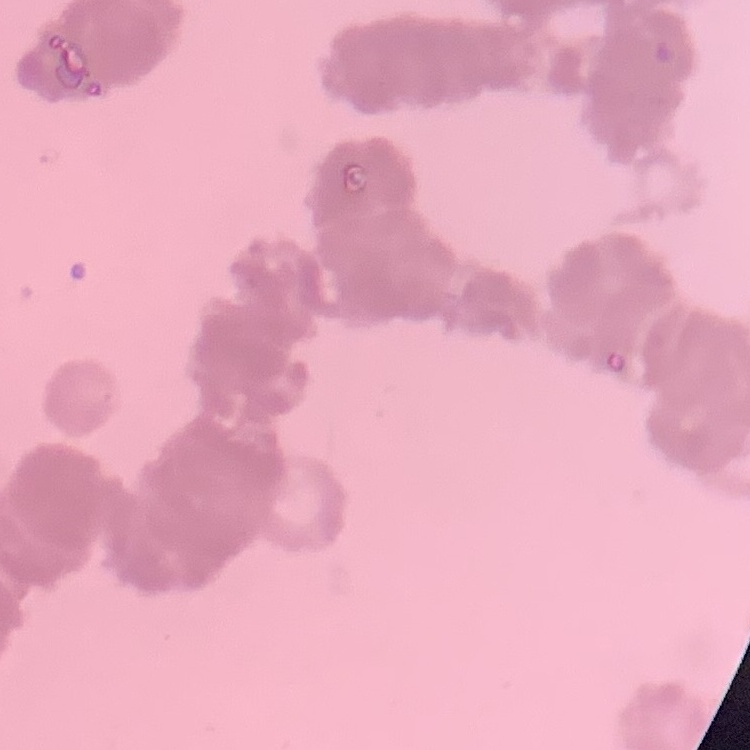
The red blood cells show rouleaux formation. One tile cut from a larger photomicrograph. Thin blood film. Field's or Giemsa stain.